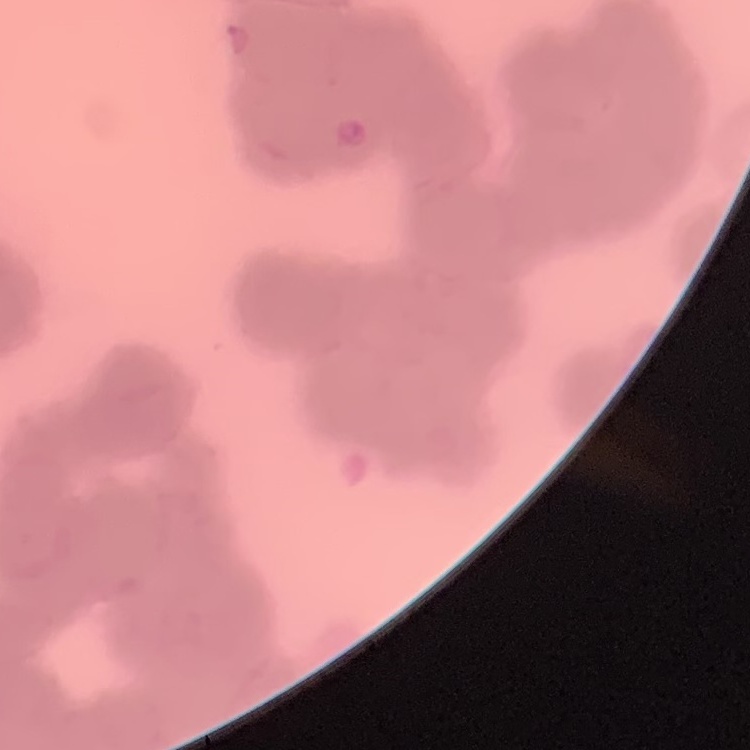

Summary:
  - Red blood cell morphology: rouleaux formation
  - Stain: Field's or Giemsa
  - Preparation: thin blood film
  - Image type: one tile cut from a larger photomicrograph